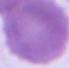
Summary:
  - Identification: red blood cell
  - Modality: photomicrograph
  - Magnification: 1000x